Locate every white blood cell.
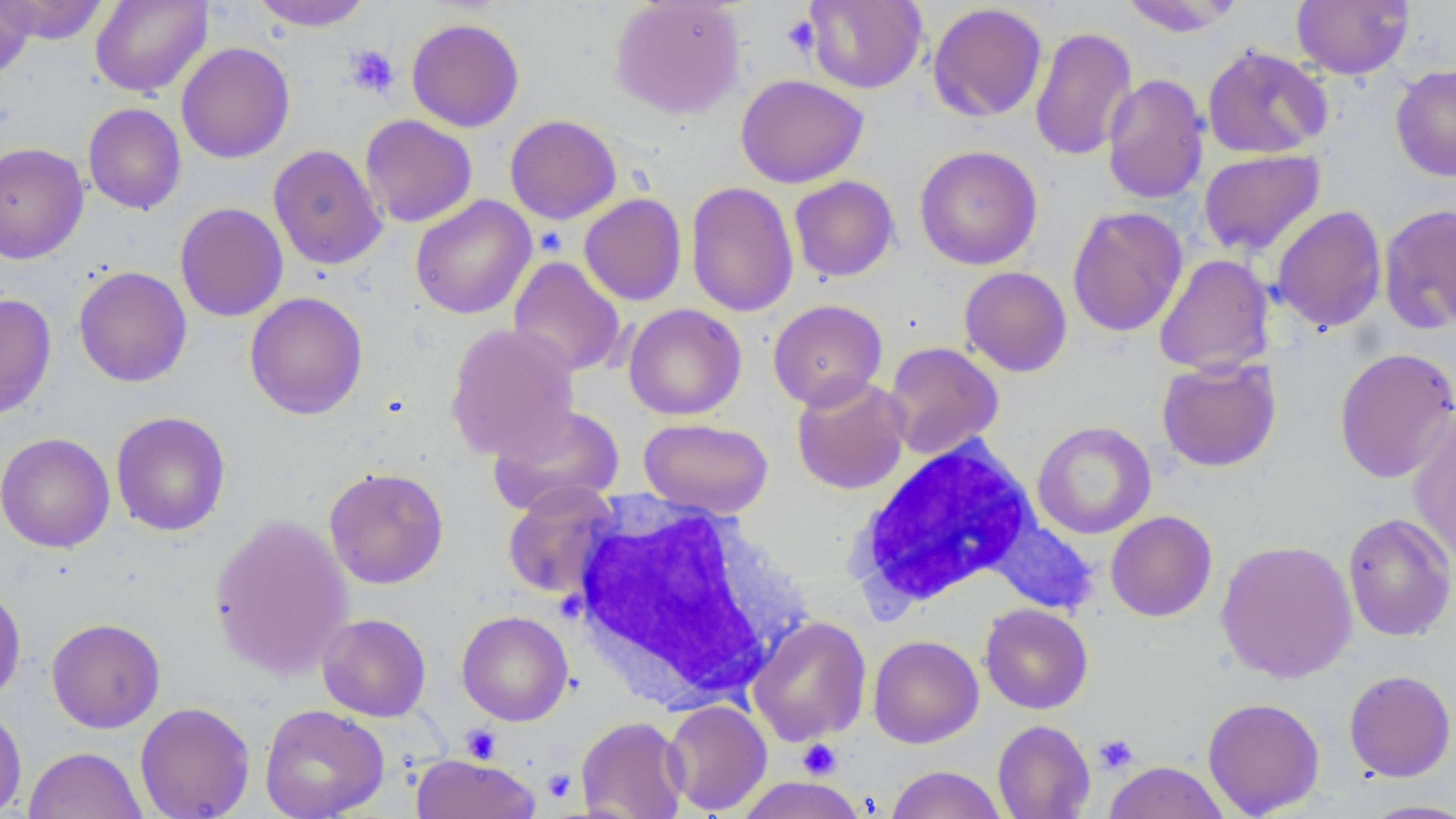

Approximate bounding boxes as named x1/y1/x2/y2 corners in pixels.
White blood cells: (x1=849, y1=437, x2=1040, y2=610), (x1=569, y1=497, x2=806, y2=707).

slide-level diagnosis = negative for blood parasites
modality = light microscopy
magnification = 1000x
stain = May-Grünwald-Giemsa
image size = 1456×819 pixels
preparation = thin blood film
field of view = one of a larger specimen
platelet locations = approximate bounding boxes as named x1/y1/x2/y2 corners in pixels: (x1=782, y1=14, x2=820, y2=57), (x1=344, y1=45, x2=399, y2=98), (x1=460, y1=725, x2=502, y2=764), (x1=1094, y1=734, x2=1138, y2=775), (x1=797, y1=738, x2=842, y2=779), (x1=542, y1=769, x2=577, y2=803)
uninfected red blood cell locations = approximate bounding boxes as named x1/y1/x2/y2 corners in pixels: (x1=1, y1=0, x2=108, y2=45), (x1=90, y1=0, x2=213, y2=98), (x1=250, y1=0, x2=373, y2=31), (x1=608, y1=0, x2=745, y2=119), (x1=1120, y1=0, x2=1245, y2=36), (x1=1291, y1=0, x2=1414, y2=79), (x1=0, y1=1, x2=36, y2=79), (x1=804, y1=1, x2=927, y2=93), (x1=927, y1=3, x2=1048, y2=122), (x1=406, y1=17, x2=524, y2=132), (x1=1029, y1=26, x2=1139, y2=162), (x1=176, y1=42, x2=295, y2=163), (x1=1202, y1=45, x2=1333, y2=159), (x1=1390, y1=64, x2=1456, y2=182), (x1=1102, y1=73, x2=1209, y2=205), (x1=735, y1=74, x2=868, y2=188), (x1=83, y1=103, x2=186, y2=215), (x1=360, y1=114, x2=477, y2=227), (x1=504, y1=115, x2=622, y2=224), (x1=0, y1=142, x2=89, y2=264), (x1=268, y1=143, x2=387, y2=270), (x1=914, y1=145, x2=1043, y2=270), (x1=1198, y1=149, x2=1326, y2=257), (x1=789, y1=176, x2=899, y2=282), (x1=685, y1=181, x2=799, y2=317), (x1=579, y1=193, x2=687, y2=306), (x1=410, y1=195, x2=536, y2=319), (x1=174, y1=203, x2=288, y2=322), (x1=1378, y1=203, x2=1456, y2=334), (x1=1271, y1=205, x2=1388, y2=333), (x1=1066, y1=206, x2=1188, y2=337), (x1=1154, y1=253, x2=1275, y2=375), (x1=508, y1=256, x2=626, y2=378), (x1=73, y1=266, x2=192, y2=387), (x1=959, y1=266, x2=1073, y2=377), (x1=244, y1=291, x2=368, y2=420), (x1=0, y1=293, x2=57, y2=420), (x1=767, y1=298, x2=888, y2=410), (x1=623, y1=303, x2=747, y2=420), (x1=444, y1=322, x2=579, y2=459), (x1=882, y1=341, x2=1004, y2=460), (x1=1333, y1=347, x2=1456, y2=483), (x1=1157, y1=357, x2=1282, y2=472), (x1=791, y1=374, x2=911, y2=495), (x1=487, y1=403, x2=625, y2=516), (x1=1408, y1=407, x2=1456, y2=565), (x1=111, y1=411, x2=231, y2=536), (x1=638, y1=417, x2=774, y2=518), (x1=1032, y1=420, x2=1156, y2=539), (x1=0, y1=432, x2=115, y2=553), (x1=323, y1=466, x2=450, y2=589), (x1=502, y1=481, x2=621, y2=600), (x1=1106, y1=511, x2=1218, y2=621), (x1=209, y1=512, x2=353, y2=680), (x1=1342, y1=512, x2=1456, y2=642), (x1=987, y1=518, x2=1099, y2=616), (x1=1215, y1=539, x2=1357, y2=684), (x1=0, y1=585, x2=26, y2=706), (x1=979, y1=603, x2=1093, y2=714), (x1=456, y1=610, x2=573, y2=726), (x1=316, y1=613, x2=431, y2=722), (x1=748, y1=615, x2=872, y2=746), (x1=47, y1=617, x2=165, y2=732), (x1=868, y1=634, x2=984, y2=748), (x1=1343, y1=669, x2=1456, y2=782), (x1=1202, y1=697, x2=1325, y2=817), (x1=662, y1=699, x2=773, y2=815), (x1=134, y1=701, x2=255, y2=818), (x1=0, y1=703, x2=27, y2=817), (x1=259, y1=703, x2=390, y2=819), (x1=576, y1=716, x2=688, y2=818), (x1=992, y1=720, x2=1095, y2=819), (x1=24, y1=746, x2=146, y2=819), (x1=410, y1=754, x2=540, y2=819), (x1=1102, y1=761, x2=1231, y2=819), (x1=886, y1=765, x2=1006, y2=818), (x1=731, y1=777, x2=871, y2=819), (x1=1358, y1=798, x2=1456, y2=818)